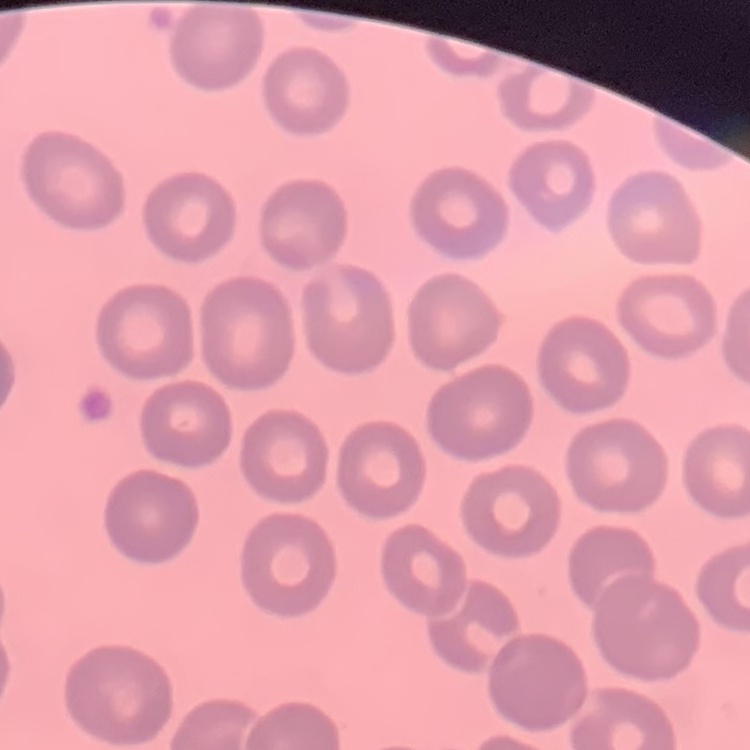
The red blood cells show no rouleaux formation. One tile cut from a larger photomicrograph. Field's or Giemsa stain. Thin blood film.